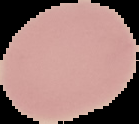 From a thin blood film. Segmented cell region on a black background. Image is 139×124 pixels. Result: no Plasmodium parasites detected.